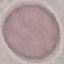

Summary:
  - Result: negative for malaria parasites
  - Capture: smartphone camera at the microscope eyepiece
  - Preparation: thin blood film
  - Stain: Giemsa
  - Image type: cell patch, automatically extracted from a larger field of view and resized to 64 × 64 pixels